State the preparation type.
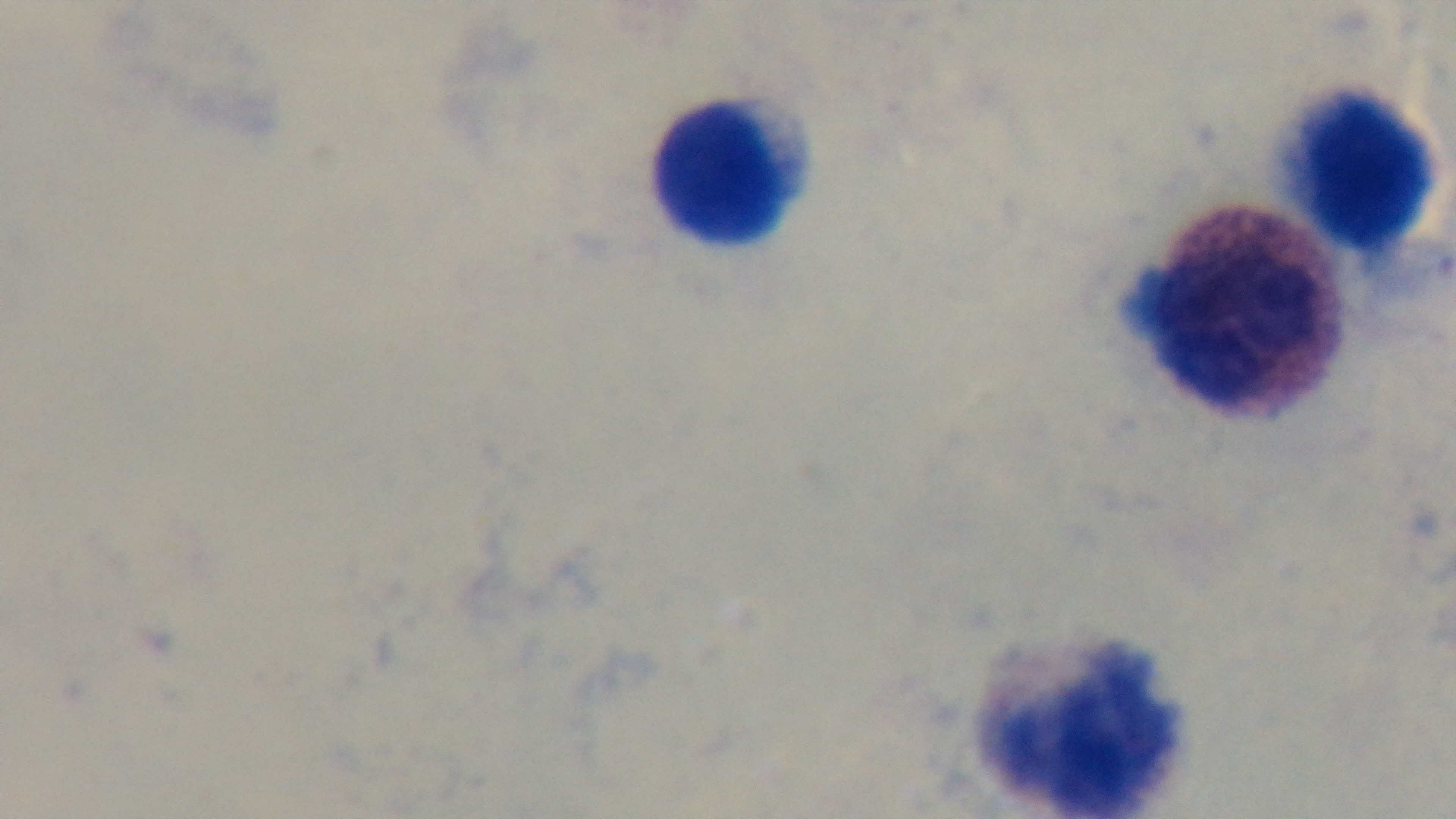
A thick smear.

Summary:
  - Stain: Giemsa
  - Capture: mounted 4K digital camera
  - Objective: 100x oil immersion
  - Malaria status: negative
  - Modality: light microscopy
  - Field of view: one from the slide